Comment on the morphology of the erythrocytes.
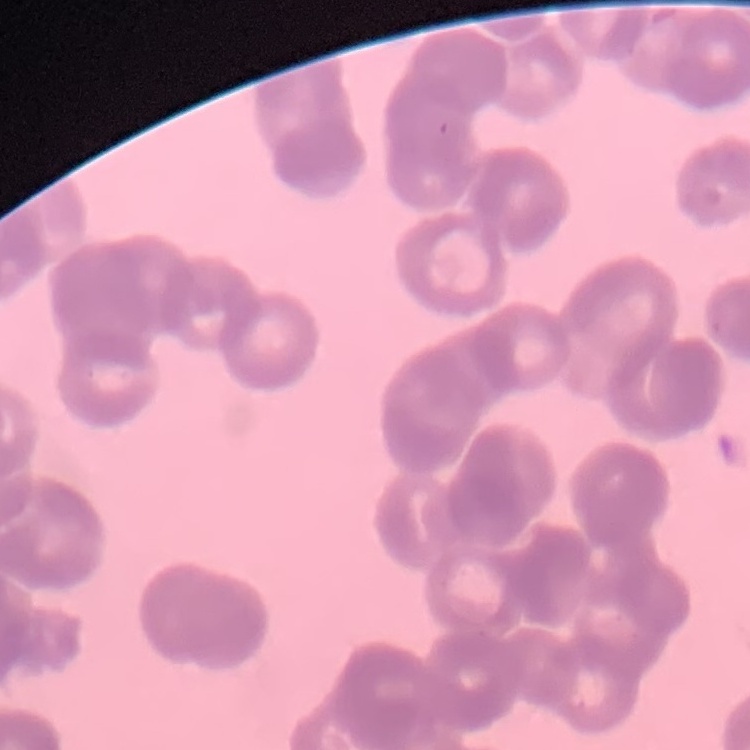

They show rouleaux formation.

stain = Field's or Giemsa
preparation = thin blood smear
image type = square crop of a larger photomicrograph